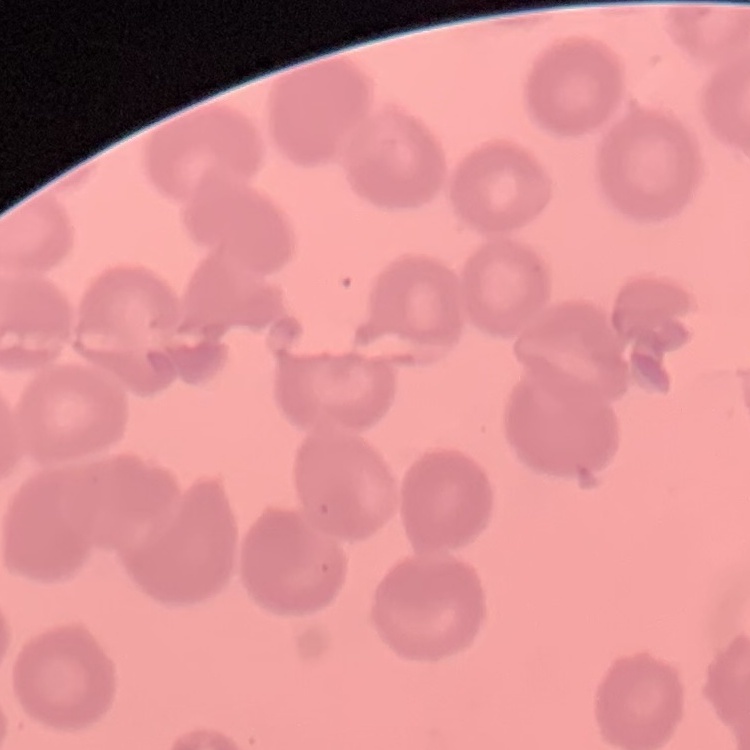

{
  "erythrocyte_morphology": "no rouleaux formation",
  "preparation": "thin blood smear",
  "image_type": "one tile cut from a larger photomicrograph",
  "stain": "Field's or Giemsa"
}